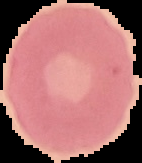

image type = segmented cell region on a black background
result = no malaria parasites detected
image size = 142×163 pixels
preparation = thin blood film